Identify the cell.
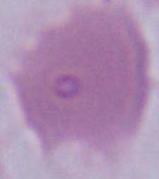

An erythrocyte.

Summary:
  - Modality: photomicrograph
  - Magnification: 1000x